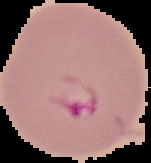

Summary:
  - Preparation: thin blood smear
  - Image size: 151×163 pixels
  - Malaria status: parasitized
  - Image type: segmented cell region with the area outside set to black